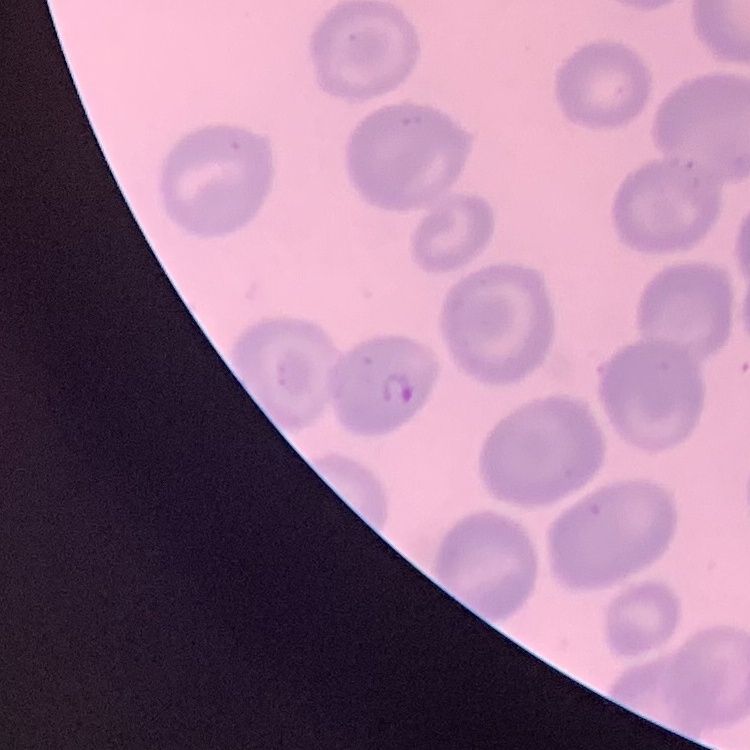

Summary:
  - Erythrocyte morphology: no rouleaux formation
  - Stain: Field's or Giemsa
  - Preparation: thin blood film
  - Image type: one tile cut from a larger photomicrograph